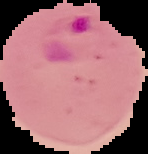 Image is 148×154 pixels. From a thin blood smear. Result: Plasmodium parasites detected. The area outside the segmented cell region is set to black.